Name the parasite shown.
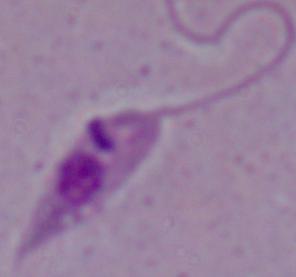

This is Leishmania.

modality: micrograph
magnification: 1000x